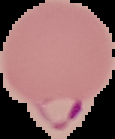

malaria status = parasitized
image size = 115×139 pixels
preparation = thin blood smear
image type = segmented cell region on a black background